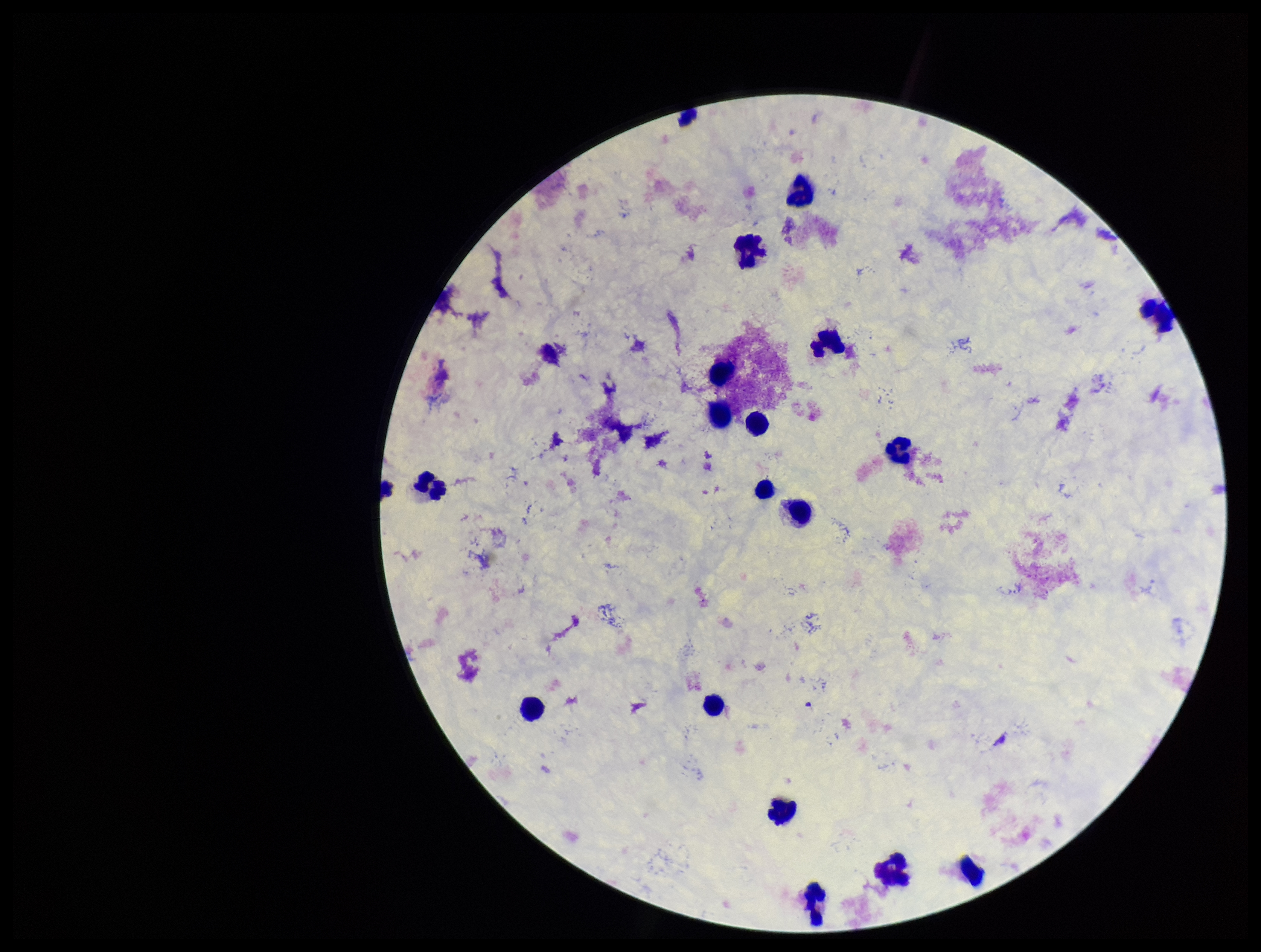
Preparation: thick blood smear. Smartphone photograph taken through the eyepiece of a microscope. Patient malaria status: negative. Parasite count: 0. Image is 1261×952 pixels. Giemsa stain. Leukocyte count: 18. One field from this slide. Plasmodium parasites: none seen.